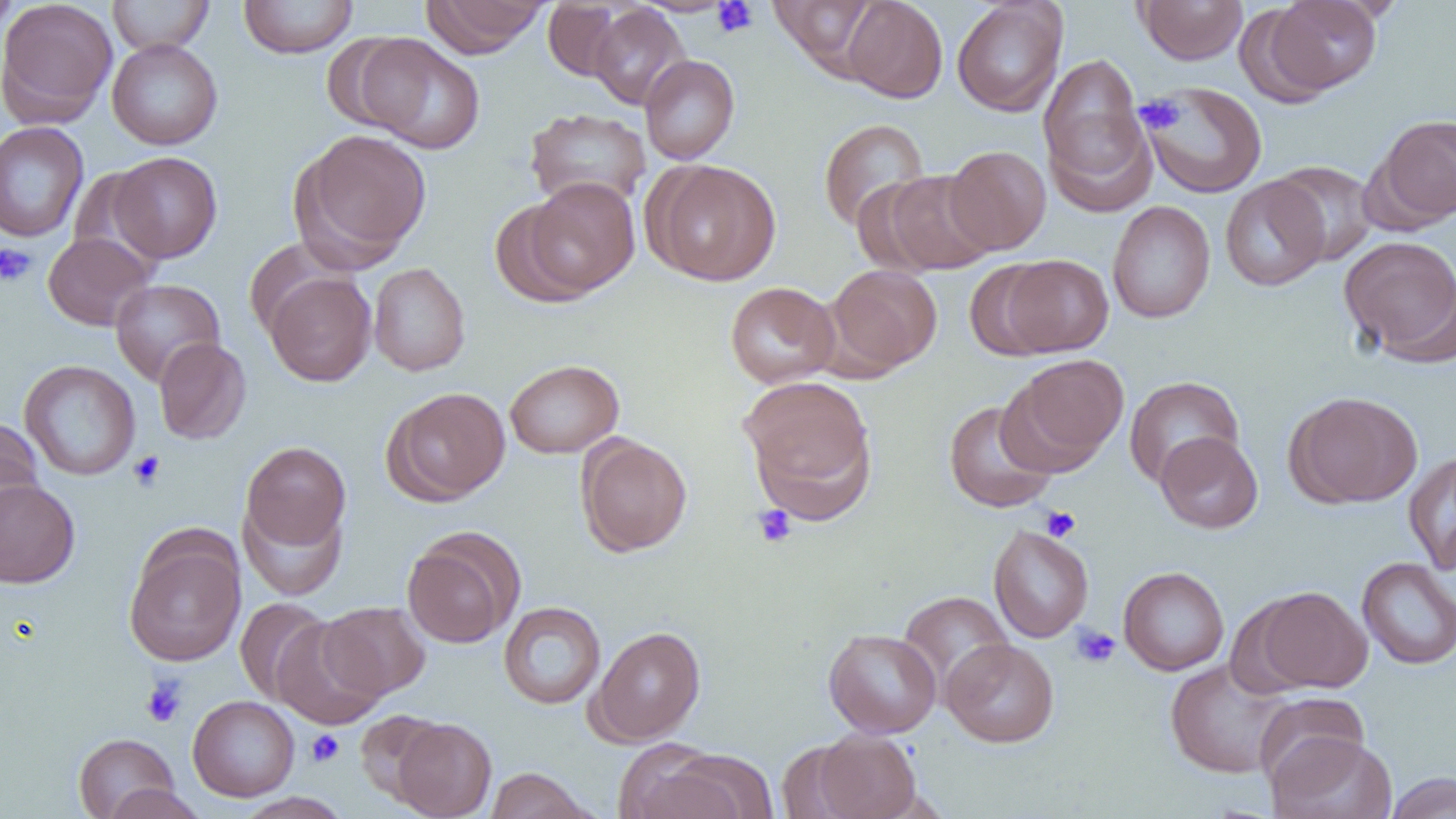

slide-level diagnosis = negative for blood parasites
image size = 1456×819 pixels
modality = light microscopy
magnification = 1000x
uninfected red blood cell locations = approximate bounding boxes as (x1, y1, x2, y2) in pixels: (0, 0, 118, 126), (108, 0, 215, 55), (239, 0, 358, 58), (421, 0, 551, 57), (842, 0, 948, 103), (951, 0, 1068, 116), (1135, 0, 1248, 65), (1263, 0, 1383, 96), (542, 1, 627, 81), (769, 1, 880, 73), (0, 2, 20, 41), (588, 4, 691, 110), (324, 32, 435, 137), (354, 34, 486, 153), (107, 38, 223, 150), (1038, 52, 1151, 200), (639, 54, 740, 165), (1140, 80, 1267, 198), (524, 107, 652, 210), (1372, 113, 1456, 225), (817, 118, 930, 232), (0, 121, 89, 243), (292, 128, 432, 267), (943, 145, 1051, 255), (108, 151, 222, 263), (646, 160, 781, 285), (1269, 160, 1380, 266), (875, 169, 998, 275), (1220, 175, 1329, 292), (518, 177, 641, 300), (1107, 200, 1216, 323), (43, 232, 155, 330), (1338, 236, 1456, 364), (242, 238, 351, 340), (1002, 254, 1114, 356), (965, 261, 1060, 361), (368, 263, 471, 376), (826, 264, 942, 374), (264, 272, 377, 386), (110, 278, 225, 386), (724, 281, 840, 388), (153, 337, 252, 445), (1009, 354, 1129, 469), (504, 359, 624, 458), (20, 360, 141, 480), (739, 376, 877, 517), (1124, 376, 1244, 487), (384, 386, 511, 505), (1286, 391, 1423, 508), (943, 399, 1058, 513), (0, 417, 45, 530), (1155, 431, 1263, 533), (576, 434, 692, 557), (240, 441, 351, 552), (1404, 451, 1456, 573), (0, 478, 81, 588), (240, 497, 347, 600), (988, 525, 1094, 643), (402, 529, 522, 648), (124, 533, 246, 666), (1357, 557, 1456, 670), (1118, 566, 1229, 675), (1251, 585, 1371, 693), (898, 590, 1014, 695), (234, 598, 333, 705), (319, 601, 431, 699), (498, 601, 606, 709), (270, 617, 387, 729), (589, 625, 706, 744), (823, 628, 942, 738), (942, 638, 1059, 747), (1164, 659, 1292, 778), (1254, 692, 1370, 791), (187, 695, 300, 801), (354, 709, 449, 808), (392, 717, 496, 818), (810, 729, 922, 819), (73, 732, 180, 818), (1268, 732, 1398, 819), (614, 740, 737, 818), (656, 748, 779, 819), (484, 767, 596, 819), (1384, 773, 1456, 819), (101, 784, 209, 819), (233, 792, 353, 819)
platelet locations = approximate bounding boxes as (x1, y1, x2, y2) in pixels: (711, 0, 758, 38), (1137, 95, 1185, 134), (0, 242, 37, 288), (128, 450, 166, 492), (752, 505, 797, 548), (1041, 506, 1081, 542), (1071, 624, 1121, 668), (141, 676, 188, 727), (306, 729, 345, 766)
field of view = one of a larger specimen
preparation = thin blood film